State which parasite is depicted.
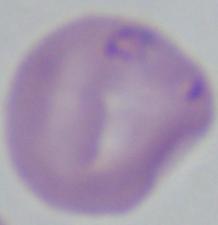
This is Babesia.

1000x magnification. Photomicrograph.